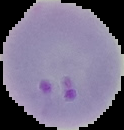

result = Plasmodium parasites identified
preparation = thin blood smear
image size = 124×130 pixels
image type = segmented cell region on a black background